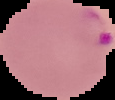 Segmented cell region on a black background. Malaria status: parasitized. Image is 115×100 pixels. From a thin blood film.